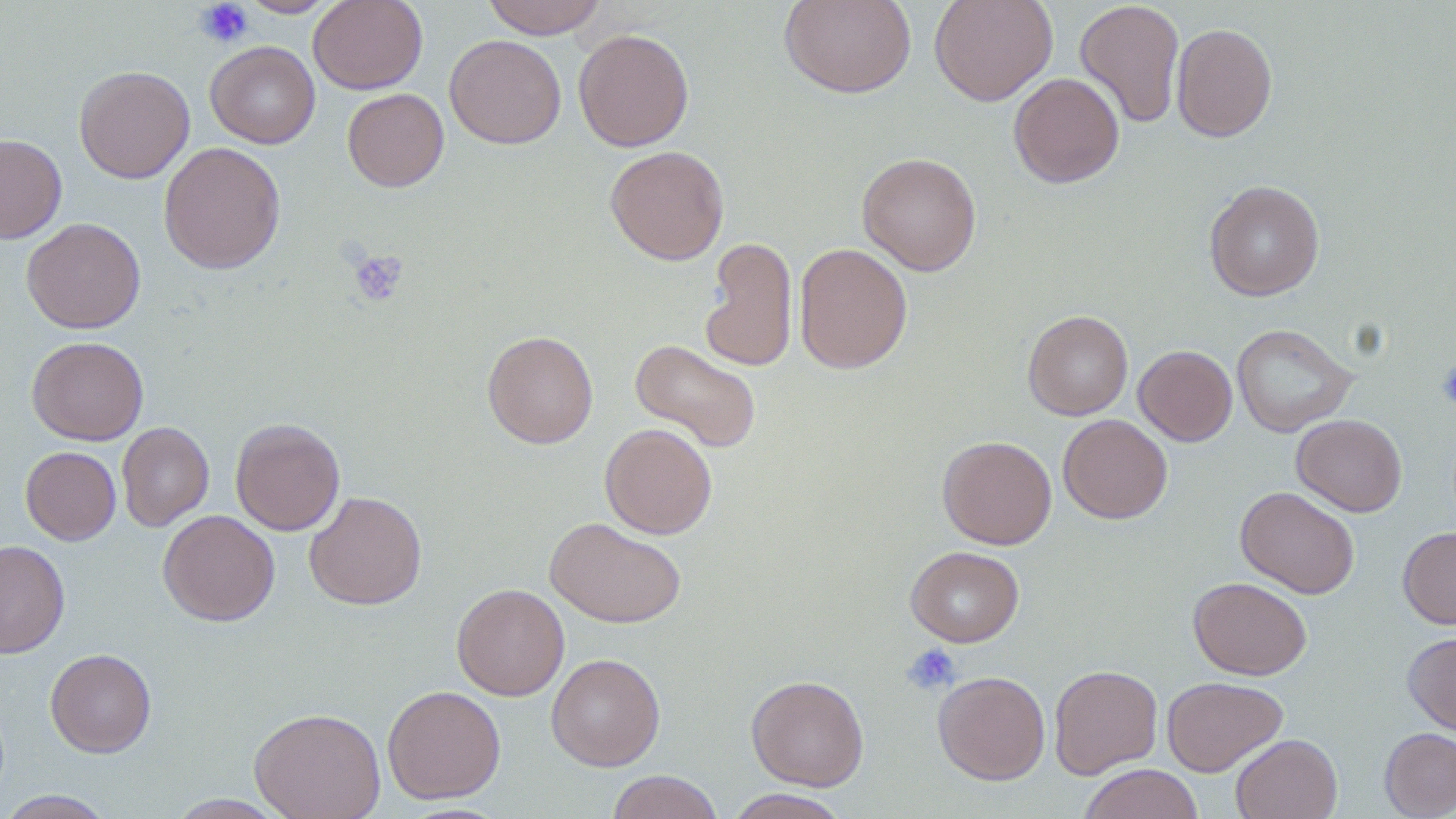
Summary:
  - Coordinate format: approximate bounding boxes as (x1,y1)-(x2,y2) corner pairs in pixels
  - Platelet locations: (194,0)-(255,48), (348,249)-(409,308), (901,643)-(961,695)
  - Uninfected red blood cell locations: (239,0)-(339,17), (308,0)-(427,94), (481,0)-(607,38), (779,0)-(917,99), (928,0)-(1058,106), (1074,0)-(1185,128), (1171,22)-(1278,142), (573,28)-(694,151), (444,34)-(567,149), (205,40)-(320,148), (74,65)-(195,183), (1008,72)-(1125,188), (342,88)-(449,192), (0,133)-(67,244), (158,142)-(286,274), (605,145)-(729,265), (857,151)-(981,275), (1204,179)-(1325,301), (22,217)-(146,334), (700,236)-(798,373), (793,242)-(912,374), (1023,310)-(1133,420), (1231,323)-(1357,437), (482,331)-(598,449), (26,336)-(149,445), (629,338)-(763,453), (1134,344)-(1237,446), (1058,414)-(1172,524), (1292,414)-(1407,517), (230,418)-(345,535), (116,421)-(214,531), (600,423)-(717,539), (937,435)-(1057,550), (20,446)-(121,545), (1235,485)-(1360,599), (304,490)-(427,610), (158,509)-(280,626), (544,516)-(687,628), (1398,526)-(1456,629), (0,539)-(70,659), (905,546)-(1024,647), (1188,576)-(1312,680), (451,582)-(569,700), (1403,630)-(1456,736), (45,648)-(157,757), (546,653)-(666,770), (1049,664)-(1163,779), (932,670)-(1050,785), (746,674)-(869,791), (1161,675)-(1288,776), (382,684)-(505,803), (249,706)-(386,819), (1379,727)-(1456,818), (1231,733)-(1342,819), (1078,764)-(1204,819), (606,770)-(725,819), (723,789)-(851,819), (0,790)-(116,818), (164,794)-(290,818)
  - Slide-level diagnosis: negative for blood parasites
  - Field of view: single
  - Modality: light microscopy
  - Preparation: thin blood film
  - Magnification: 1000x
  - Stain: May-Grünwald-Giemsa
  - Image size: 1456×819 pixels